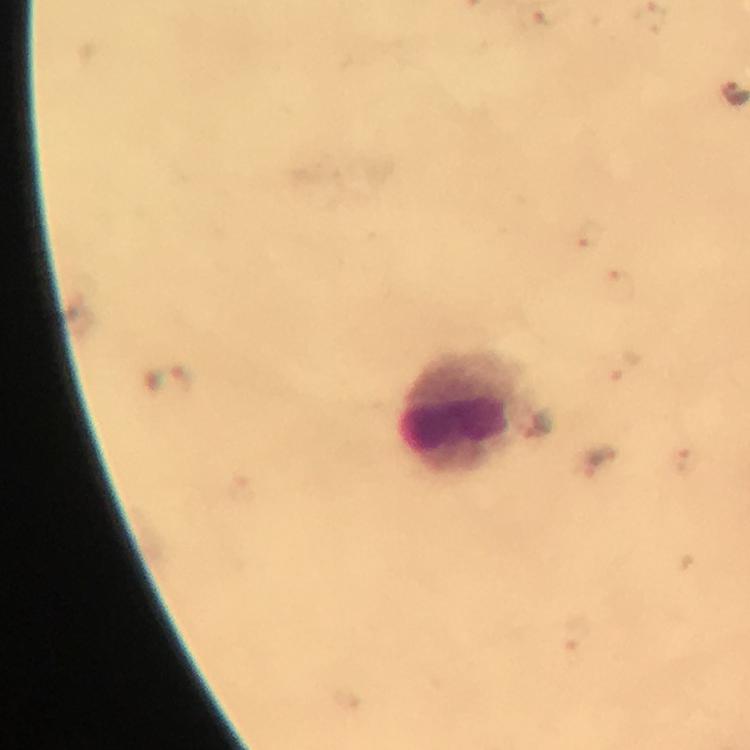
Approximate object centers, in pixels from the top-left corner. Malaria parasite locations: (x=169, y=384). Leukocyte locations: (x=466, y=413). 100x magnification. From a malaria diagnostic workup. A crop from one field of view. Image is 750×750 pixels. Thick smear. Immersion oil was used. Giemsa-stained preparation. Photographed through the microscope with a smartphone camera.